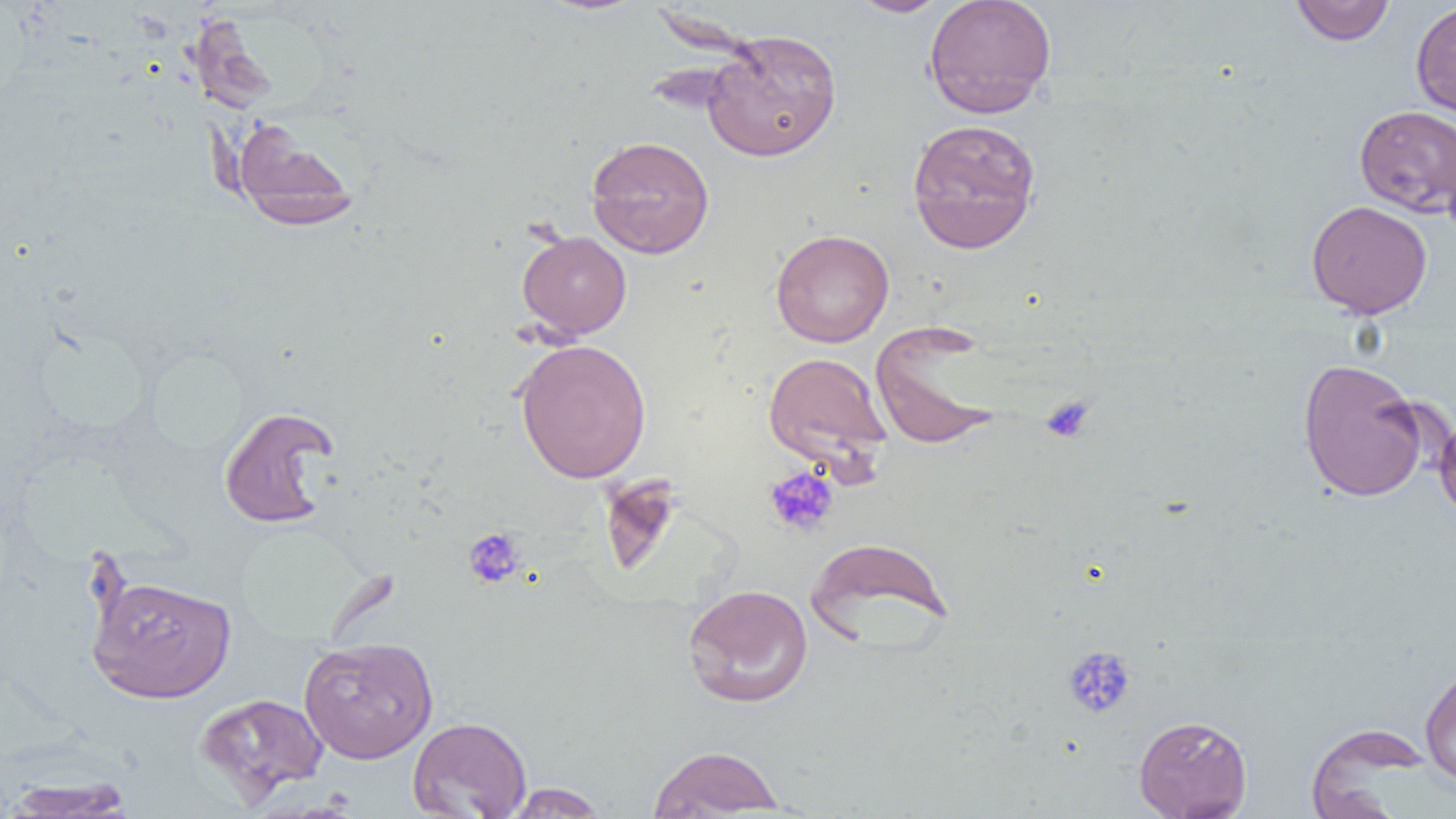 Approximate bounding boxes as (x1, y1, x2, y2) in pixels. Uninfected red blood cell locations: (845, 0, 953, 17), (924, 0, 1057, 118), (1290, 1, 1396, 46), (1410, 1, 1456, 121), (187, 12, 278, 115), (702, 29, 842, 162), (1354, 105, 1456, 216), (231, 116, 361, 230), (907, 117, 1041, 254), (586, 135, 715, 258), (1306, 200, 1432, 319), (770, 229, 894, 348), (517, 230, 631, 340), (870, 322, 1003, 450), (514, 338, 652, 483), (763, 352, 892, 469), (1297, 358, 1430, 502), (218, 405, 340, 529), (1434, 405, 1456, 523), (806, 536, 953, 648), (86, 573, 236, 703), (682, 583, 813, 707), (299, 635, 439, 763), (1420, 664, 1456, 785), (195, 692, 329, 803), (1133, 714, 1252, 819), (407, 716, 531, 818), (1305, 723, 1431, 817), (647, 745, 786, 817), (0, 777, 136, 818), (504, 783, 609, 818). Platelet locations: (1040, 396, 1096, 443), (763, 465, 839, 536), (462, 527, 526, 589), (1062, 645, 1136, 718). Slide-level diagnosis: negative for blood parasites. Optical microscopy. Image is 1456×819 pixels. One field of a larger specimen. Thin blood smear. 1000x magnification.